Assess the morphology of the red blood cells.
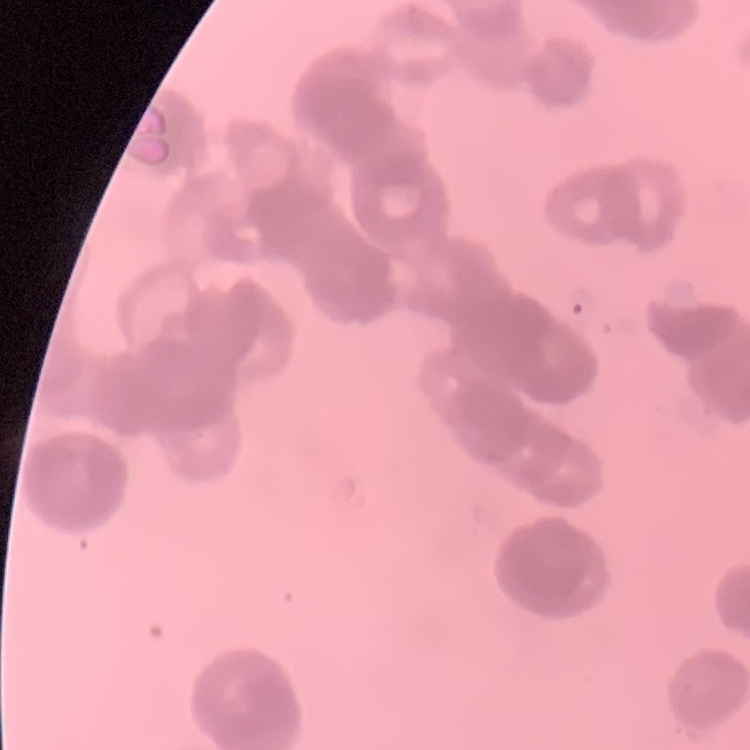

They show rouleaux formation.

image type = one tile cut from a larger photomicrograph
preparation = thin blood smear
stain = Field's or Giemsa